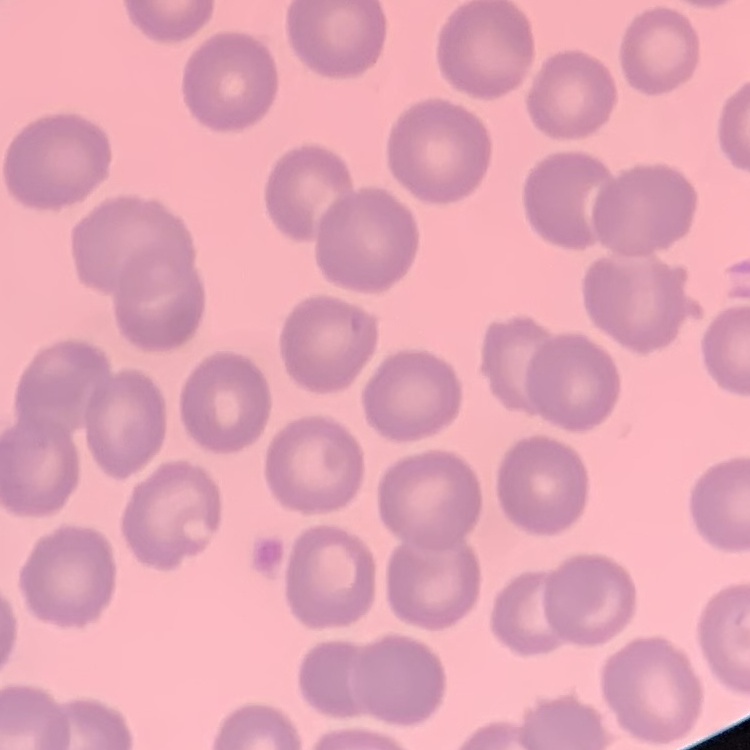

red blood cell morphology = no rouleaux formation
preparation = thin blood smear
image type = square crop of a larger photomicrograph
stain = Field's or Giemsa